Point out each Plasmodium parasite and each leukocyte.
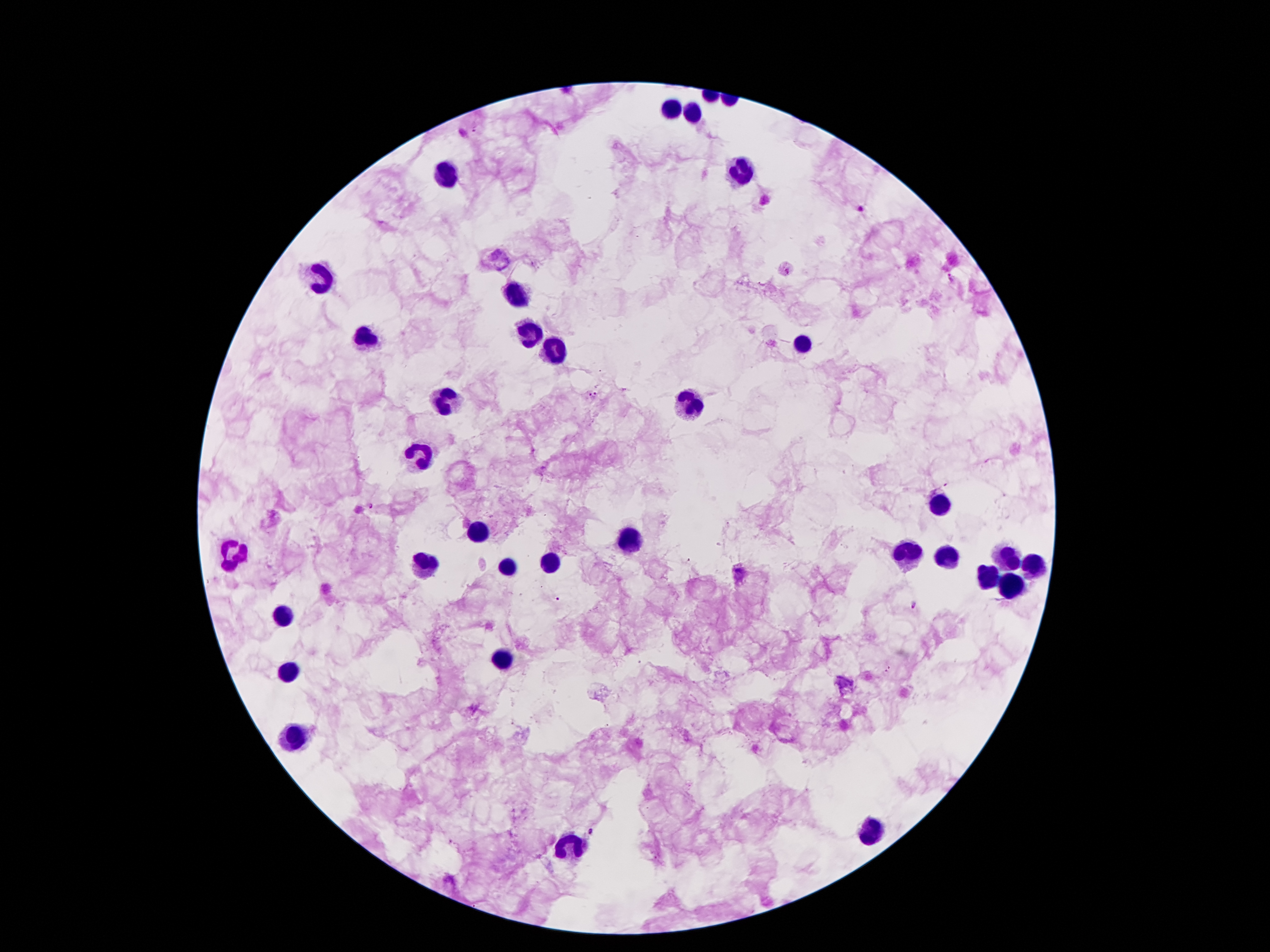

Approximate object centers, in pixels from the top-left corner.
Plasmodium parasites: (x=476, y=129), (x=463, y=134), (x=859, y=210), (x=788, y=271), (x=593, y=394), (x=372, y=507), (x=740, y=571), (x=914, y=605), (x=888, y=669), (x=590, y=831).
Leukocytes: (x=671, y=109), (x=694, y=114), (x=740, y=169), (x=446, y=175), (x=323, y=277), (x=515, y=298), (x=529, y=332), (x=366, y=338), (x=802, y=345), (x=556, y=354), (x=445, y=402), (x=691, y=405), (x=421, y=453), (x=941, y=505), (x=479, y=531), (x=630, y=538), (x=231, y=552), (x=906, y=555), (x=947, y=557), (x=1005, y=557), (x=550, y=564), (x=425, y=566), (x=1028, y=567), (x=509, y=570), (x=989, y=576), (x=1012, y=587), (x=280, y=616), (x=506, y=659), (x=288, y=671), (x=297, y=736), (x=871, y=830), (x=572, y=845).

preparation = thick blood smear
image size = 1270×952 pixels
stain = Giemsa
magnification = 100x
capture = smartphone through the microscope eyepiece
patient malaria status = infected with Plasmodium falciparum
field of view = single